Describe the morphology of the erythrocytes.
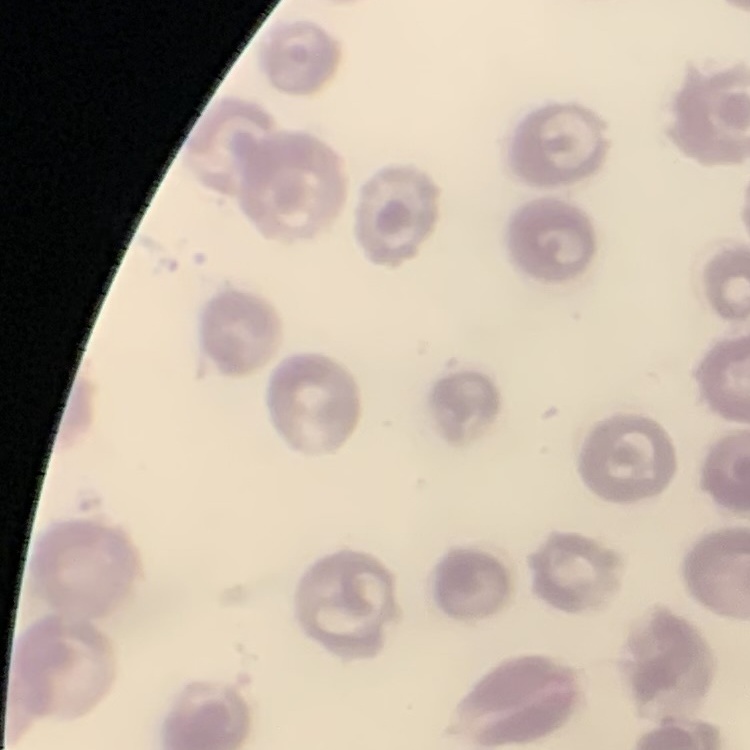
No rouleaux formation.

Summary:
  - Stain: Field's or Giemsa
  - Preparation: thin blood film
  - Image type: one tile cut from a larger photomicrograph